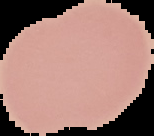

Summary:
  - Image size: 154×136 pixels
  - Result: no malaria parasites detected
  - Preparation: thin blood film
  - Image type: segmented cell region on a black background